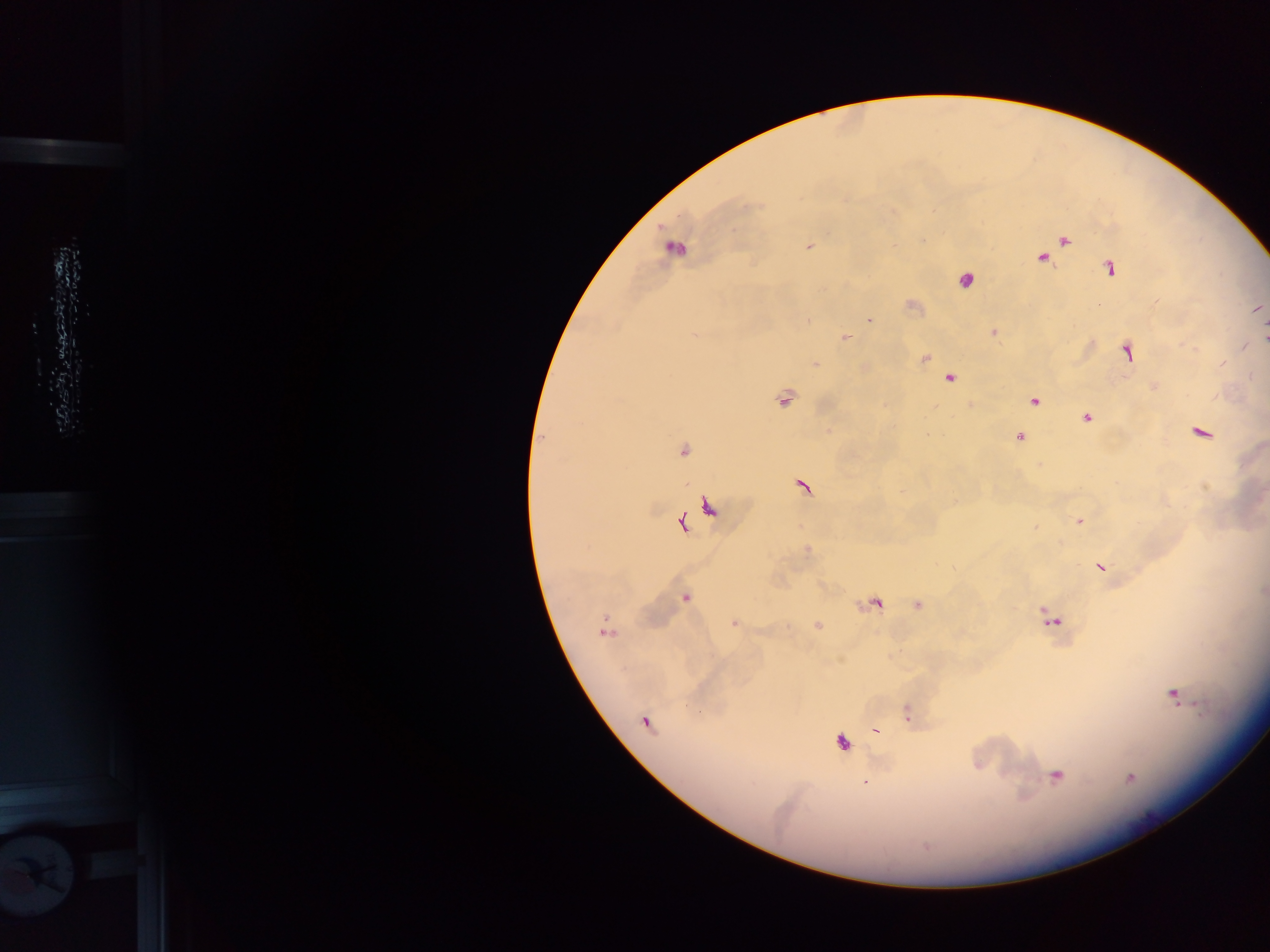

country: Ghana
plasmodium_parasite_locations: 'approximate centers as [x, y] in pixels: [1063, 240], [808, 247], [673, 248], [1042, 257], [1109, 268], [964, 280], [912, 305], [1256, 309], [869, 320], [993, 332], [845, 338], [1264, 338], [1243, 346], [1126, 352], [924, 358], [815, 363], [863, 368], [948, 378], [1155, 386], [783, 398], [1033, 400], [971, 405], [1086, 416], [1200, 432], [1018, 437], [682, 450], [803, 486], [709, 507], [1079, 520], [681, 522], [807, 549], [1101, 567], [1263, 592], [685, 597], [874, 603], [918, 604], [1049, 618], [734, 623], [818, 625], [605, 629], [1173, 694], [907, 713], [646, 721], [875, 731], [841, 741], [1056, 775], [1129, 778], [864, 783]'
image_size: 1270×952 pixels
capture: mobile-phone photograph through a microscope
field_of_view: single
preparation: thick blood film